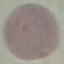
result = negative for malaria parasites
stain = Giemsa
capture = smartphone camera at the microscope eyepiece
image type = automatically extracted cell patch, resized to 64 × 64 pixels
preparation = thin blood smear